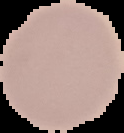

Summary:
  - Preparation: thin blood film
  - Image size: 124×133 pixels
  - Image type: cell region segmented out of the field of view; surrounding area masked to black
  - Result: no Plasmodium parasites seen